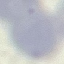 Malaria status: uninfected. Photographed with a smartphone camera at the microscope eyepiece. Giemsa-stained preparation. Thin blood smear. Cell patch, automatically extracted from a larger field of view and resized to 64 × 64 pixels.